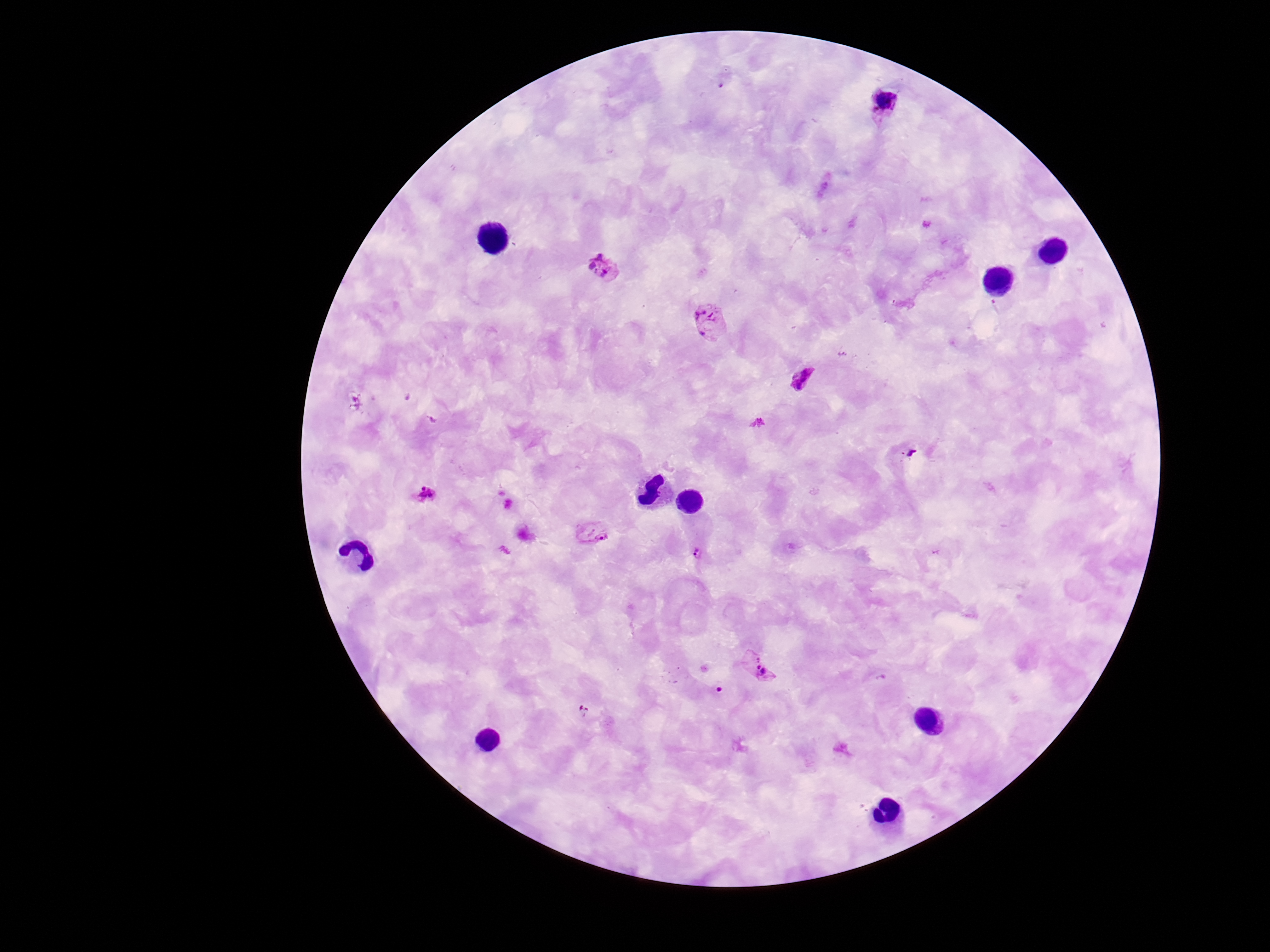 Approximate centers as {x, y} in pixels. Plasmodium parasite locations: {884, 106}, {603, 268}, {709, 322}, {802, 378}, {427, 496}, {591, 531}, {697, 554}, {759, 667}, {584, 712}. Photographed through the microscope eyepiece with a smartphone camera. Image is 1270×952 pixels. Patient malaria status: positive. One field from this slide. Thick blood smear. Giemsa-stained preparation. 100x magnification.